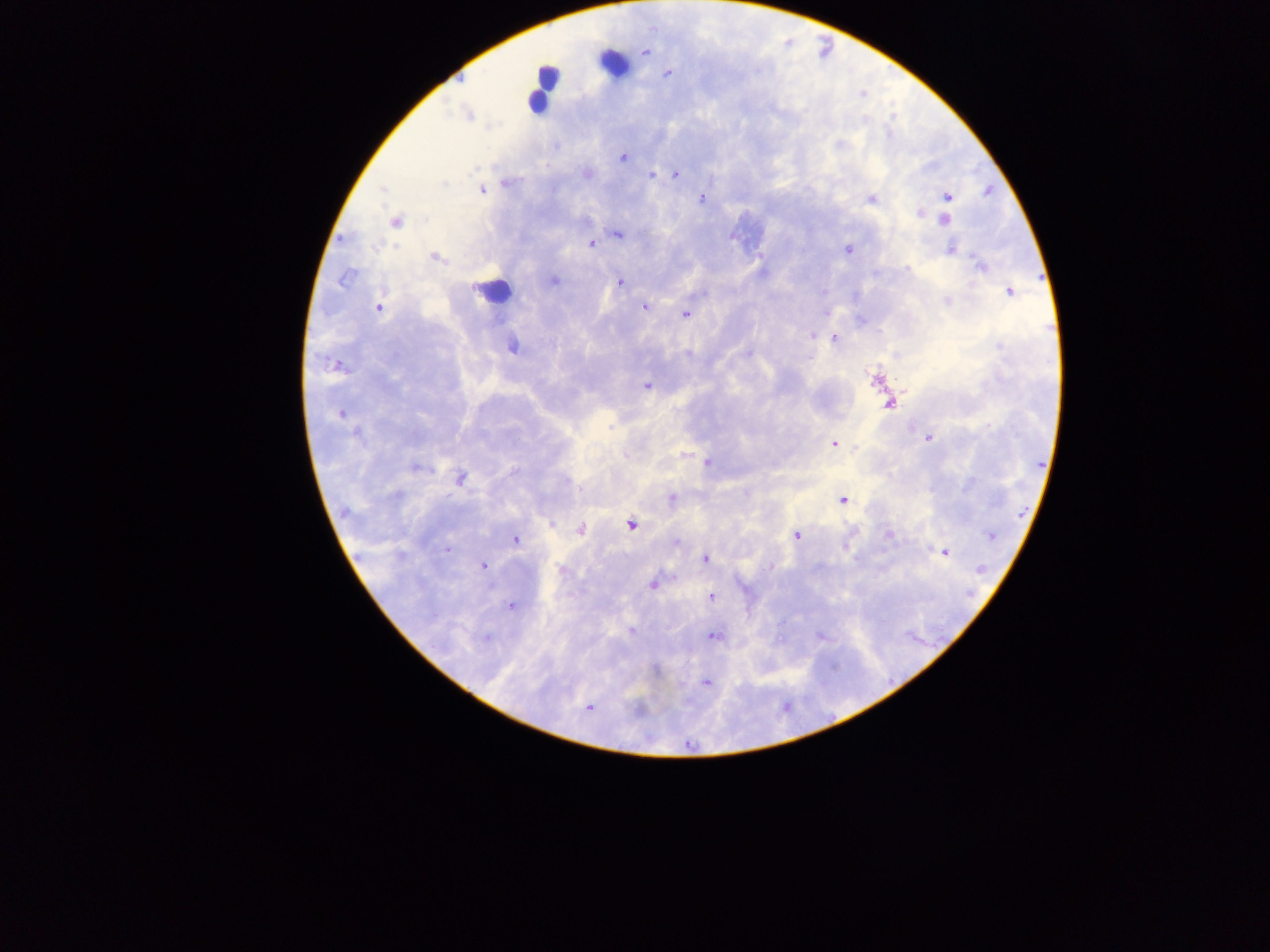
Approximate centers as [x, y] in pixels.
Summary:
  - Plasmodium parasite locations: [669, 76], [458, 83], [862, 96], [469, 113], [623, 157], [654, 174], [675, 174], [507, 182], [443, 185], [381, 190], [481, 190], [989, 190], [949, 196], [702, 198], [872, 199], [919, 212], [945, 219], [395, 222], [618, 233], [343, 240], [378, 244], [591, 244], [395, 246], [952, 247], [847, 248], [435, 259], [979, 264], [346, 278], [555, 279], [622, 283], [1010, 291], [947, 300], [644, 307], [378, 308], [685, 314], [815, 334], [834, 337], [747, 352], [338, 366], [648, 386], [890, 404], [424, 414], [340, 415], [610, 426], [357, 433], [929, 438], [835, 443], [707, 462], [419, 467], [460, 480], [844, 499], [552, 522], [631, 526], [581, 529], [798, 535], [890, 536], [990, 537], [516, 538], [448, 550], [945, 552], [705, 558], [483, 566], [982, 570], [655, 583], [710, 596], [513, 606], [631, 632], [713, 637], [707, 683], [591, 707]
  - Preparation: thick blood smear
  - Country: Ghana
  - Field of view: single
  - Capture: mobile-phone photograph through a microscope
  - Image size: 1270×952 pixels